Classify this cell by malaria status.
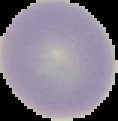
It is uninfected.

Image is 118×121 pixels. From a thin blood film. Cell region segmented out of the field of view; the surrounding area is masked to black.